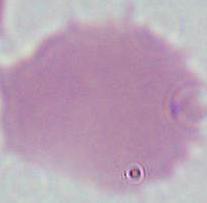
magnification = 1000x
modality = micrograph
identification = erythrocyte